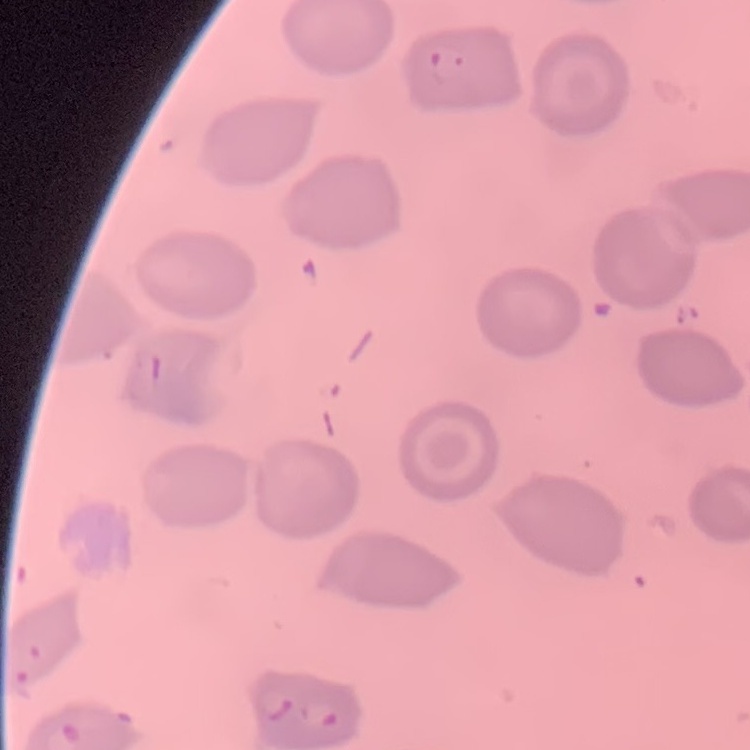
Summary:
  - Erythrocyte morphology: no rouleaux formation
  - Image type: square crop of a larger photomicrograph
  - Preparation: thin blood smear
  - Stain: Field's or Giemsa